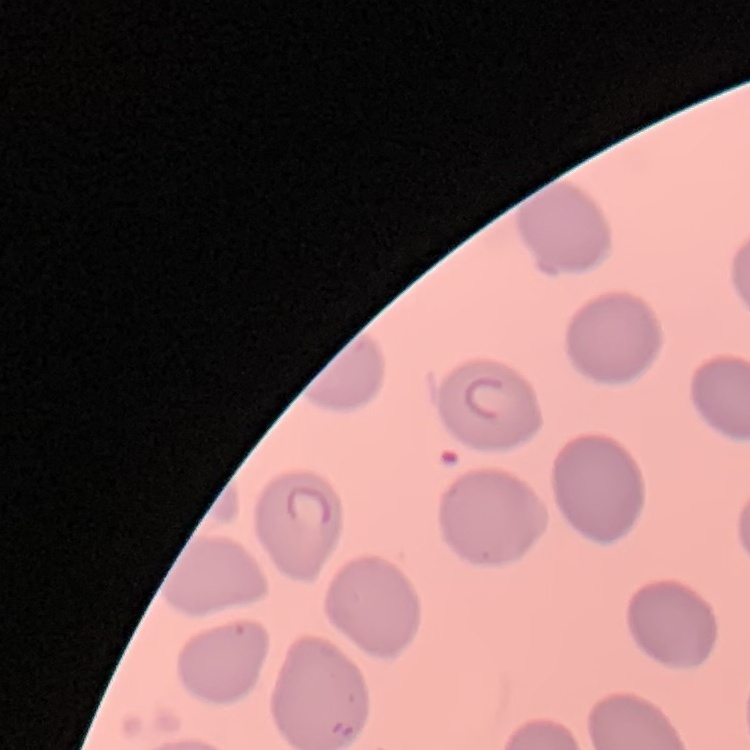
red_blood_cell_morphology: no rouleaux formation
preparation: thin blood smear
image_type: square crop of a larger photomicrograph
stain: Field's or Giemsa